Assess this cell for malaria.
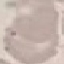
Uninfected.

Summary:
  - Preparation: thin smear
  - Image type: cell patch, automatically extracted from a larger field of view and resized to 64 × 64 pixels
  - Stain: Giemsa
  - Capture: smartphone through the microscope eyepiece